Locate every Plasmodium parasite.
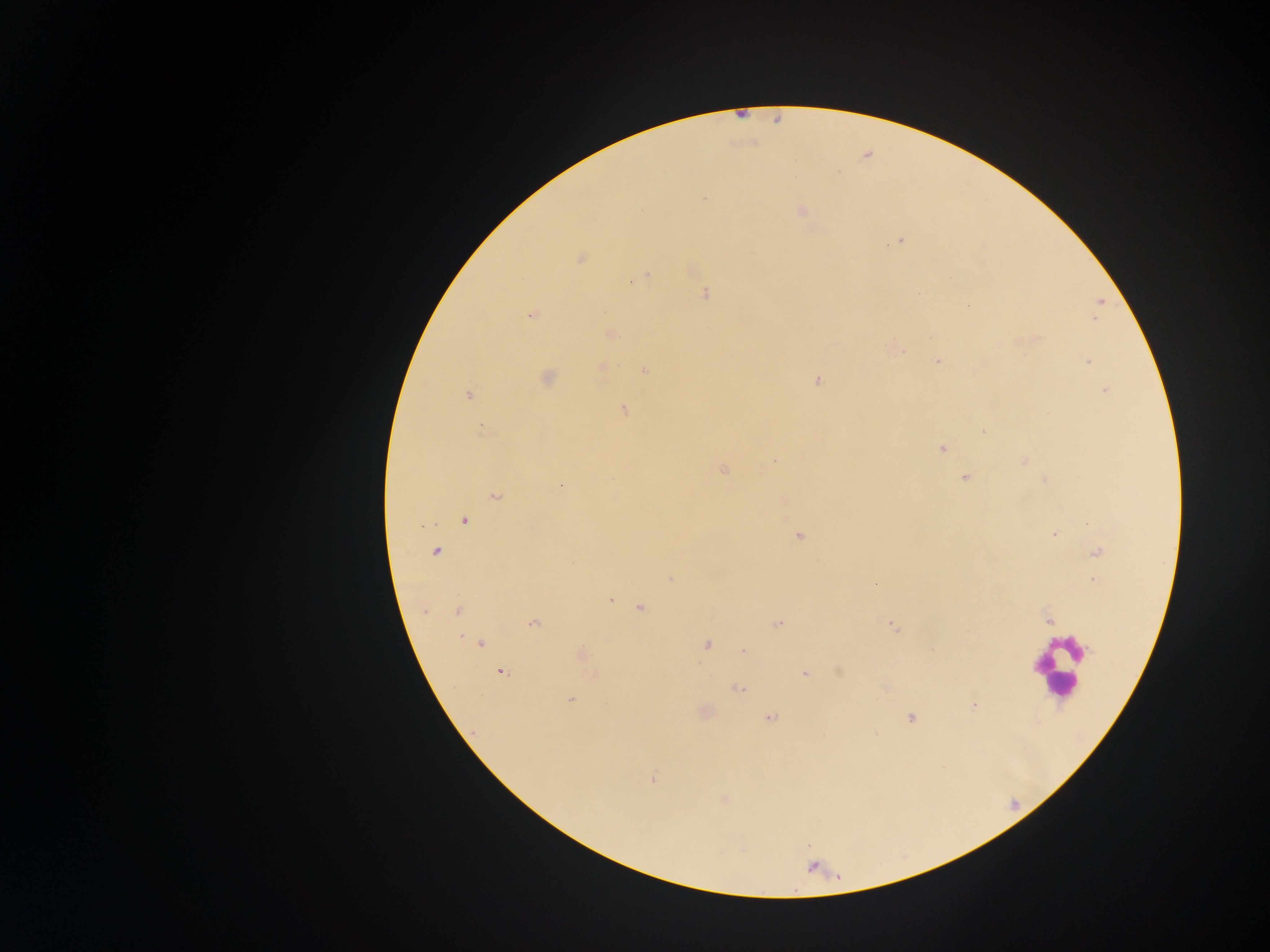
Approximate centers as {x, y} in pixels.
Plasmodium parasites: {703, 199}, {801, 211}, {899, 240}, {580, 258}, {690, 267}, {646, 276}, {705, 294}, {1100, 301}, {531, 315}, {610, 334}, {894, 349}, {937, 359}, {1087, 360}, {602, 367}, {645, 370}, {547, 377}, {817, 381}, {1106, 390}, {468, 395}, {623, 409}, {481, 429}, {983, 432}, {941, 448}, {773, 460}, {1024, 460}, {723, 469}, {965, 478}, {1045, 480}, {560, 486}, {494, 496}, {783, 501}, {463, 520}, {1053, 534}, {799, 535}, {435, 551}, {1097, 551}, {670, 578}, {1093, 579}, {874, 582}, {609, 599}, {641, 606}, {424, 610}, {458, 610}, {1048, 620}, {533, 622}, {776, 624}, {892, 624}, {479, 643}, {706, 645}, {744, 651}, {581, 655}, {500, 671}, {838, 671}, {805, 674}, {739, 688}, {571, 700}, {973, 705}, {703, 711}, {769, 717}, {910, 717}, {653, 779}, {724, 799}.

Leukocyte locations: {1058, 667}. Mobile-phone photograph taken through the microscope. Single field of view. Thick blood film. Sample from Ghana. Image is 1270×952 pixels.